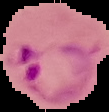

image type = cell region segmented out of the field of view; surrounding area masked to black
preparation = thin blood smear
malaria status = parasitized
image size = 109×112 pixels